Outline each blood parasite and name the species.
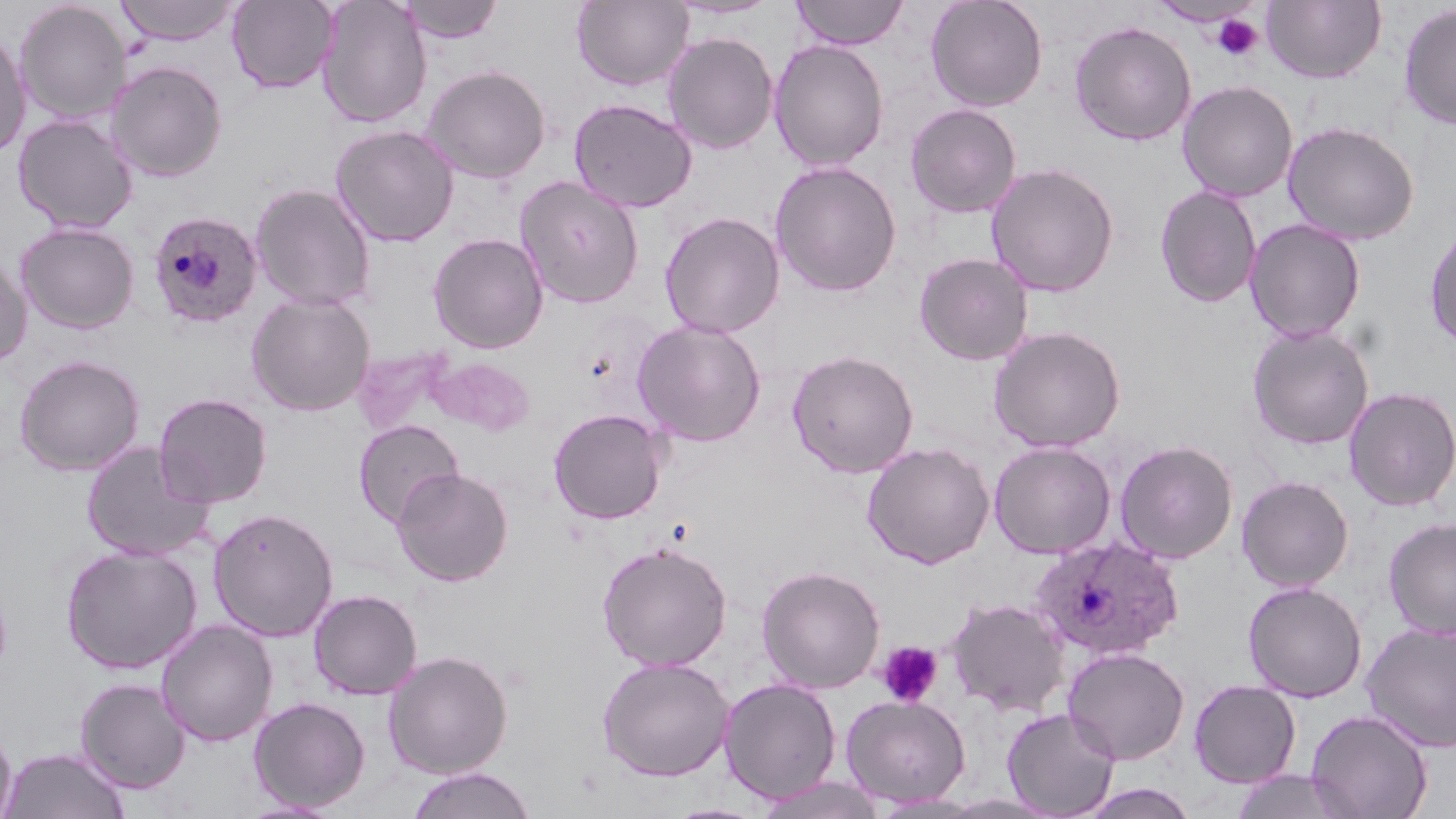

Approximate bounding boxes as [x1, y1, x2, y2] in pixels.
Plasmodium ovale-infected red blood cells: [147, 209, 262, 329], [1028, 534, 1184, 661].
No Plasmodium falciparum, Plasmodium malariae, Plasmodium vivax, Babesia divergens, or Trypanosoma brucei observed.

Uninfected red blood cell locations: [316, 0, 432, 129], [395, 0, 505, 43], [572, 0, 694, 92], [664, 0, 781, 20], [790, 0, 909, 50], [925, 0, 1048, 112], [1261, 0, 1387, 84], [14, 1, 131, 125], [114, 1, 241, 46], [226, 1, 339, 93], [1398, 3, 1456, 130], [1069, 21, 1196, 146], [0, 28, 32, 160], [663, 32, 778, 154], [769, 39, 889, 171], [106, 61, 228, 182], [421, 64, 551, 183], [1177, 80, 1298, 202], [568, 98, 698, 213], [904, 103, 1021, 218], [13, 114, 138, 233], [1282, 121, 1420, 245], [330, 124, 459, 247], [770, 160, 902, 297], [985, 162, 1120, 298], [515, 176, 645, 309], [250, 183, 376, 311], [1154, 185, 1263, 308], [659, 211, 785, 338], [1244, 219, 1366, 343], [1424, 220, 1456, 352], [15, 222, 139, 333], [428, 232, 549, 354], [0, 252, 32, 367], [914, 253, 1034, 365], [246, 293, 375, 416], [631, 318, 767, 446], [1246, 323, 1376, 450], [988, 325, 1125, 452], [351, 345, 455, 438], [787, 349, 919, 478], [14, 354, 145, 476], [427, 356, 535, 436], [1343, 386, 1456, 511], [153, 392, 273, 508], [548, 408, 669, 524], [353, 419, 464, 527], [1115, 440, 1238, 563], [80, 441, 215, 561], [988, 441, 1116, 559], [861, 442, 995, 569], [391, 466, 513, 586], [1236, 475, 1355, 591], [208, 507, 339, 641], [1383, 517, 1456, 639], [596, 541, 732, 672], [60, 543, 202, 674], [756, 565, 885, 693], [1242, 581, 1368, 702], [308, 589, 422, 700], [946, 597, 1070, 716], [156, 619, 278, 747], [1361, 622, 1456, 753], [1062, 646, 1190, 764], [383, 650, 513, 778], [596, 656, 734, 781], [75, 677, 190, 793], [718, 677, 841, 805], [1188, 679, 1301, 787], [841, 694, 971, 807], [248, 696, 371, 812], [1002, 707, 1120, 818], [1305, 709, 1433, 819], [0, 721, 16, 819], [1, 746, 131, 818], [404, 766, 538, 818], [1228, 769, 1359, 819], [757, 776, 886, 818], [1074, 783, 1201, 819], [870, 794, 987, 818], [933, 794, 1062, 818], [235, 799, 345, 819], [664, 802, 769, 819]. Platelet locations: [1211, 14, 1264, 61], [0, 595, 13, 670], [876, 641, 944, 707]. Slide-level diagnosis: Plasmodium ovale. Light microscopy. May-Grünwald-Giemsa-stained preparation. Image is 1456×819 pixels. One field of a larger specimen. Thin blood film. Captured at 1000x magnification.